Assess this cell for malaria.
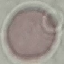
Uninfected.

stain = Giemsa
preparation = thin smear
capture = smartphone through the microscope eyepiece
image type = automatically extracted cell patch, resized to 64 × 64 pixels